Identify the cell.
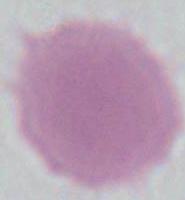

This is an erythrocyte.

Photomicrograph. 1000x magnification.